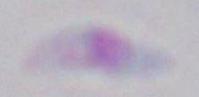
Summary:
  - Magnification: 1000x
  - Identification: Toxoplasma gondii
  - Modality: micrograph